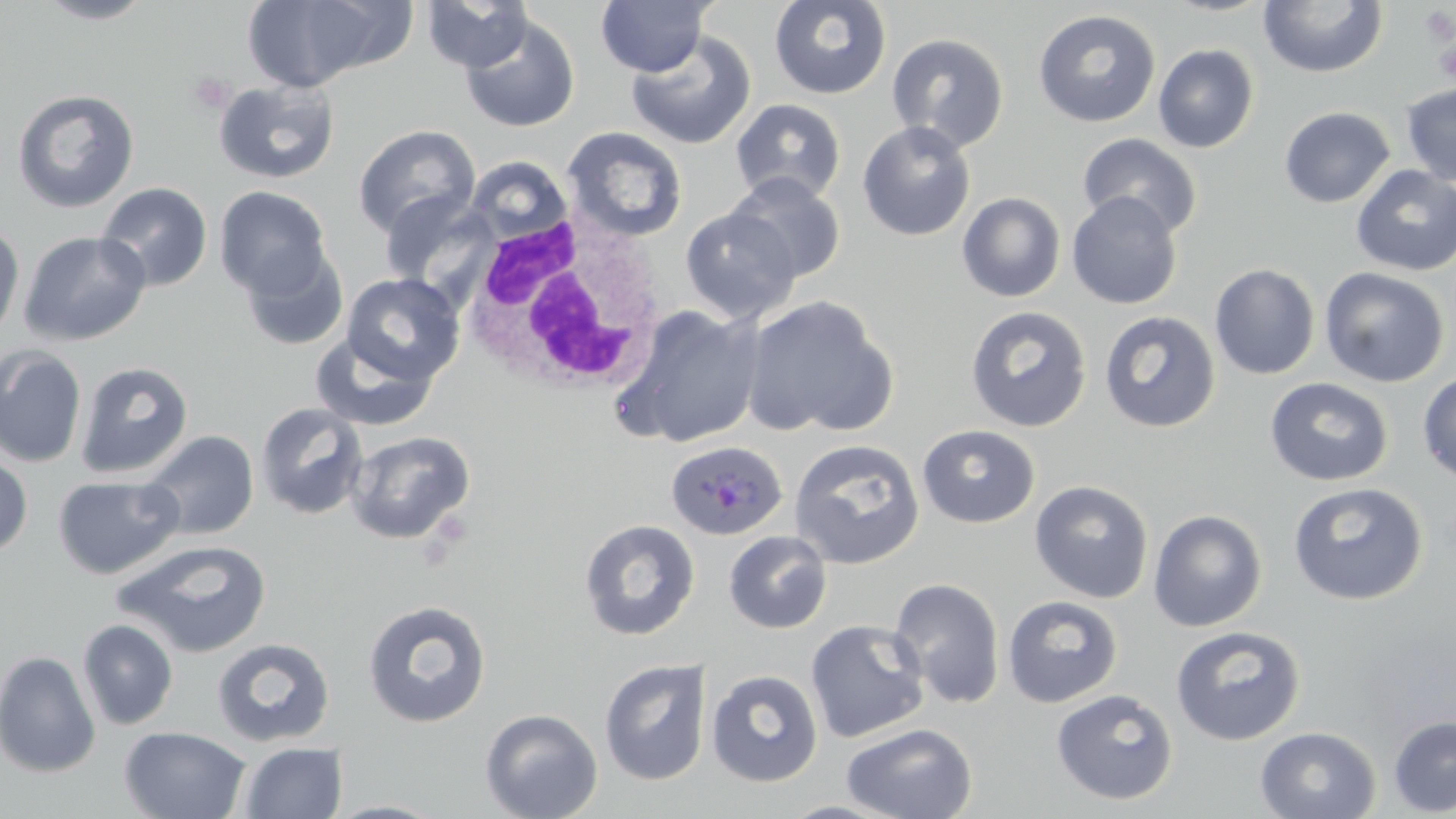

Summary:
  - Coordinate format: approximate bounding boxes as (x1, y1, x2, y2) in pixels
  - Platelet locations: (1419, 5, 1456, 44), (1434, 37, 1456, 85), (186, 72, 235, 115)
  - White blood cell locations: (458, 212, 667, 397)
  - Plasmodium ovale-infected red blood cell locations: (665, 441, 788, 541)
  - Uninfected red blood cell locations: (34, 0, 158, 25), (240, 0, 403, 93), (420, 0, 534, 72), (596, 0, 713, 77), (769, 0, 892, 100), (1258, 0, 1387, 78), (1033, 9, 1161, 127), (459, 13, 580, 133), (625, 31, 757, 150), (886, 32, 1010, 153), (1153, 44, 1259, 153), (213, 80, 340, 184), (1401, 83, 1456, 188), (11, 88, 140, 213), (731, 99, 846, 205), (1279, 106, 1395, 208), (857, 120, 976, 241), (353, 125, 481, 239), (561, 126, 689, 242), (1078, 133, 1203, 239), (465, 155, 572, 243), (1351, 165, 1456, 276), (725, 173, 846, 284), (96, 182, 213, 292), (214, 185, 332, 298), (379, 189, 493, 291), (1066, 191, 1183, 309), (957, 192, 1066, 303), (680, 206, 802, 324), (0, 220, 25, 344), (19, 230, 152, 347), (241, 245, 349, 351), (1209, 263, 1320, 379), (1319, 267, 1450, 388), (341, 272, 464, 386), (741, 294, 897, 437), (618, 304, 765, 449), (965, 305, 1092, 432), (1099, 311, 1221, 433), (310, 327, 440, 432), (0, 345, 87, 468), (74, 361, 194, 479), (1418, 371, 1456, 483), (1264, 377, 1393, 486), (255, 402, 369, 520), (917, 424, 1040, 528), (141, 430, 259, 540), (346, 430, 475, 545), (788, 439, 925, 569), (0, 452, 33, 559), (53, 475, 185, 579), (1029, 479, 1154, 603), (1288, 481, 1428, 605), (1148, 509, 1267, 632), (579, 518, 701, 641), (724, 530, 832, 634), (112, 539, 272, 657), (889, 577, 1006, 709), (1002, 595, 1123, 708), (362, 600, 491, 728), (77, 619, 179, 730), (805, 619, 930, 743), (1170, 625, 1307, 746), (211, 637, 336, 748), (0, 650, 102, 778), (599, 658, 710, 786), (706, 669, 824, 787), (1051, 688, 1178, 805), (480, 708, 603, 819), (1388, 715, 1456, 816), (841, 722, 977, 819), (119, 726, 251, 819), (1255, 726, 1381, 819), (237, 741, 347, 818), (323, 799, 451, 818)
  - Slide-level diagnosis: Plasmodium ovale
  - Stain: May-Grünwald-Giemsa
  - Modality: optical microscopy
  - Image size: 1456×819 pixels
  - Preparation: thin blood film
  - Field of view: single
  - Magnification: 1000x